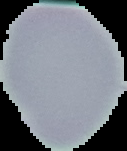
Summary:
  - Image size: 127×151 pixels
  - Image type: cell region segmented out of the field of view; surrounding area masked to black
  - Preparation: thin blood film
  - Malaria status: uninfected